Classify this cell by malaria status.
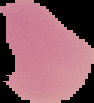
Uninfected.

Cell region segmented out of the field of view; the surrounding area is masked to black. Image is 94×103 pixels. From a thin blood film.